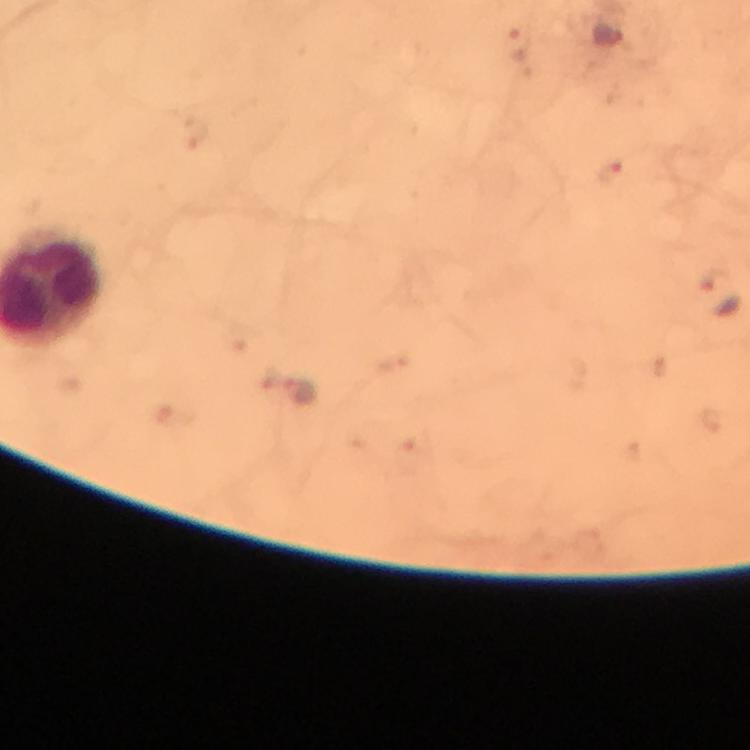
{
  "immersion_oil": "applied",
  "context": "from a diagnostic examination for malaria",
  "preparation": "thick blood smear",
  "malaria_parasite_locations": "approximate object centers, in pixels from the top-left corner: (x=607, y=35), (x=520, y=45), (x=612, y=173)",
  "image_size": "750×750 pixels",
  "stain": "Giemsa",
  "cropped_from": "one field of view",
  "magnification": "100x",
  "capture": "smartphone photograph through a microscope"
}